Locate and identify every blood parasite.
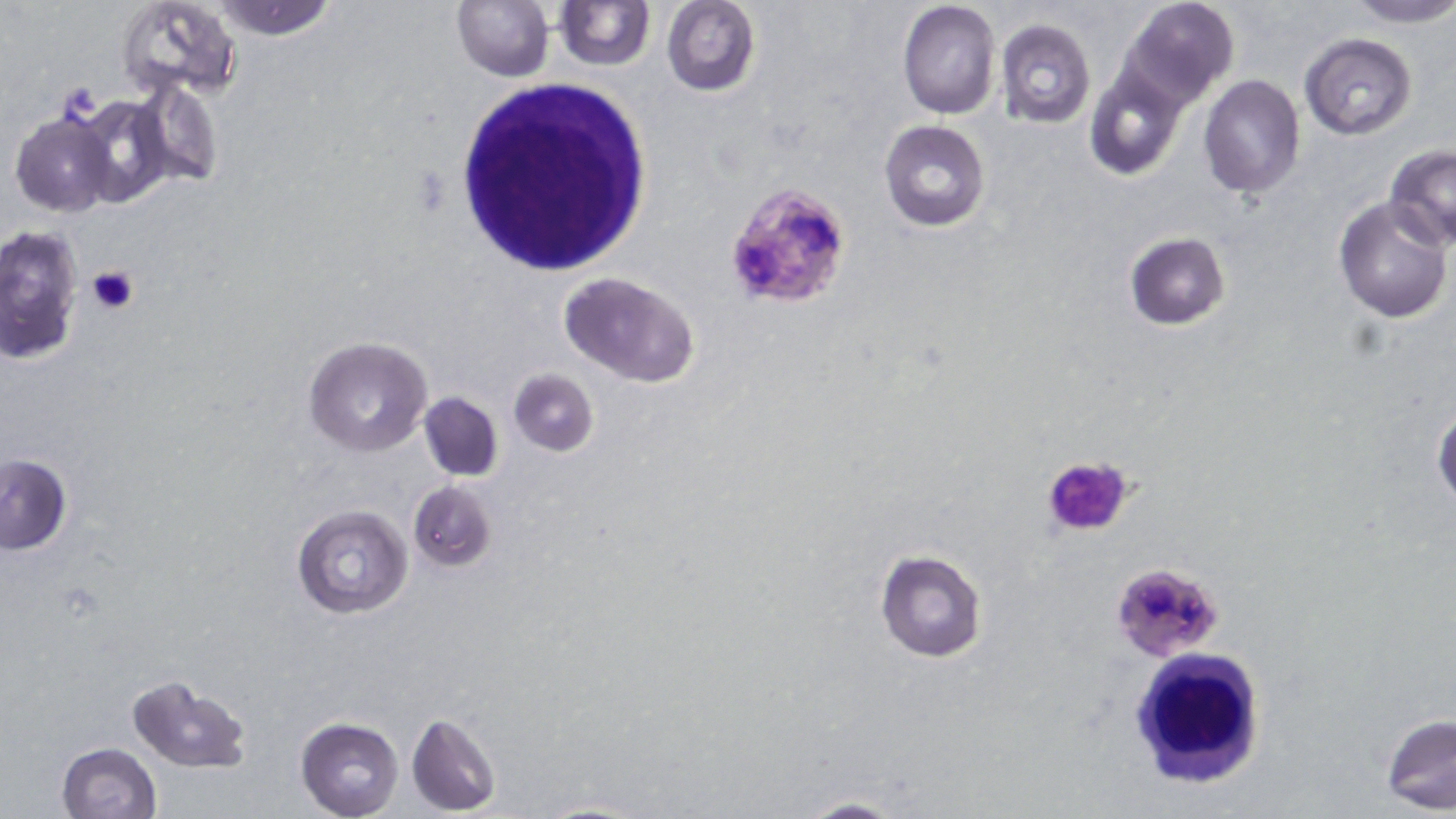
Approximate bounding boxes as (x1, y1, x2, y2) in pixels.
Plasmodium falciparum-infected red blood cells: (724, 180, 852, 309), (1109, 563, 1224, 661).
No Plasmodium ovale, Plasmodium malariae, Plasmodium vivax, Babesia divergens, or Trypanosoma brucei observed.

Summary:
  - Platelet locations: (86, 265, 138, 316), (1042, 454, 1133, 538)
  - White blood cell locations: (452, 79, 654, 274), (1126, 649, 1266, 791)
  - Uninfected red blood cell locations: (116, 0, 241, 101), (211, 0, 338, 41), (452, 0, 554, 82), (556, 0, 654, 69), (897, 0, 1001, 119), (1122, 0, 1240, 106), (1343, 0, 1456, 28), (661, 1, 760, 96), (995, 18, 1097, 130), (1299, 34, 1417, 140), (1083, 59, 1191, 183), (1197, 74, 1306, 198), (130, 77, 224, 189), (68, 95, 176, 209), (9, 110, 118, 217), (879, 120, 991, 232), (1384, 144, 1456, 248), (1332, 195, 1454, 323), (0, 224, 83, 366), (1125, 232, 1231, 330), (558, 273, 700, 386), (302, 336, 433, 456), (509, 368, 599, 456), (418, 391, 505, 482), (1431, 399, 1456, 509), (0, 455, 73, 556), (409, 480, 496, 572), (292, 505, 414, 620), (875, 548, 988, 662), (124, 674, 254, 772), (1379, 712, 1456, 813), (405, 713, 500, 815), (296, 716, 405, 819), (56, 742, 163, 819), (787, 796, 911, 819), (529, 797, 655, 819)
  - Slide-level diagnosis: Plasmodium falciparum
  - Field of view: single
  - Modality: light microscopy
  - Magnification: 1000x
  - Preparation: thin blood smear
  - Stain: May-Grünwald-Giemsa
  - Image size: 1456×819 pixels